Comment on the morphology of the red blood cells.
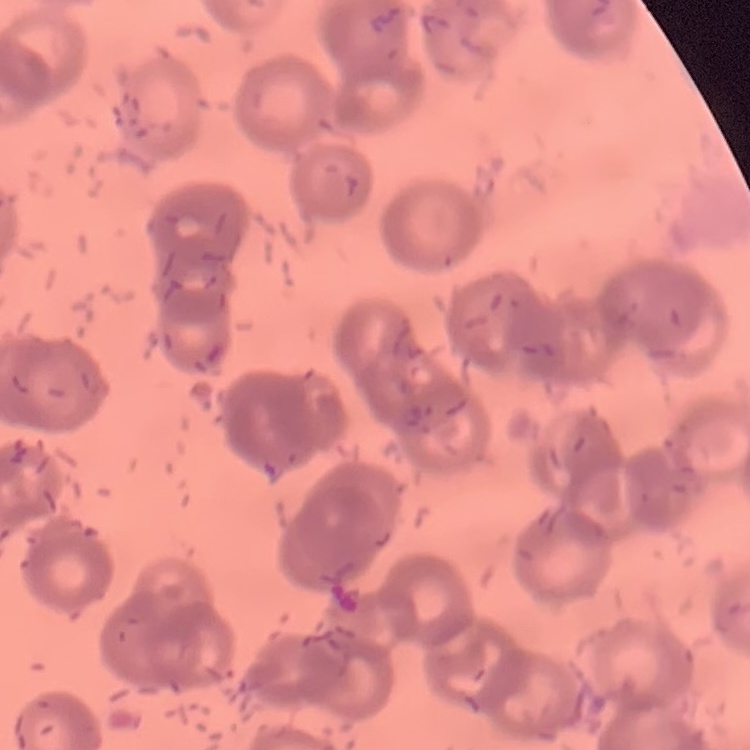
They show rouleaux formation.

Summary:
  - Stain: Field's or Giemsa
  - Image type: square crop of a larger photomicrograph
  - Preparation: thin peripheral smear